Give the extent of all uninfected red blood cells.
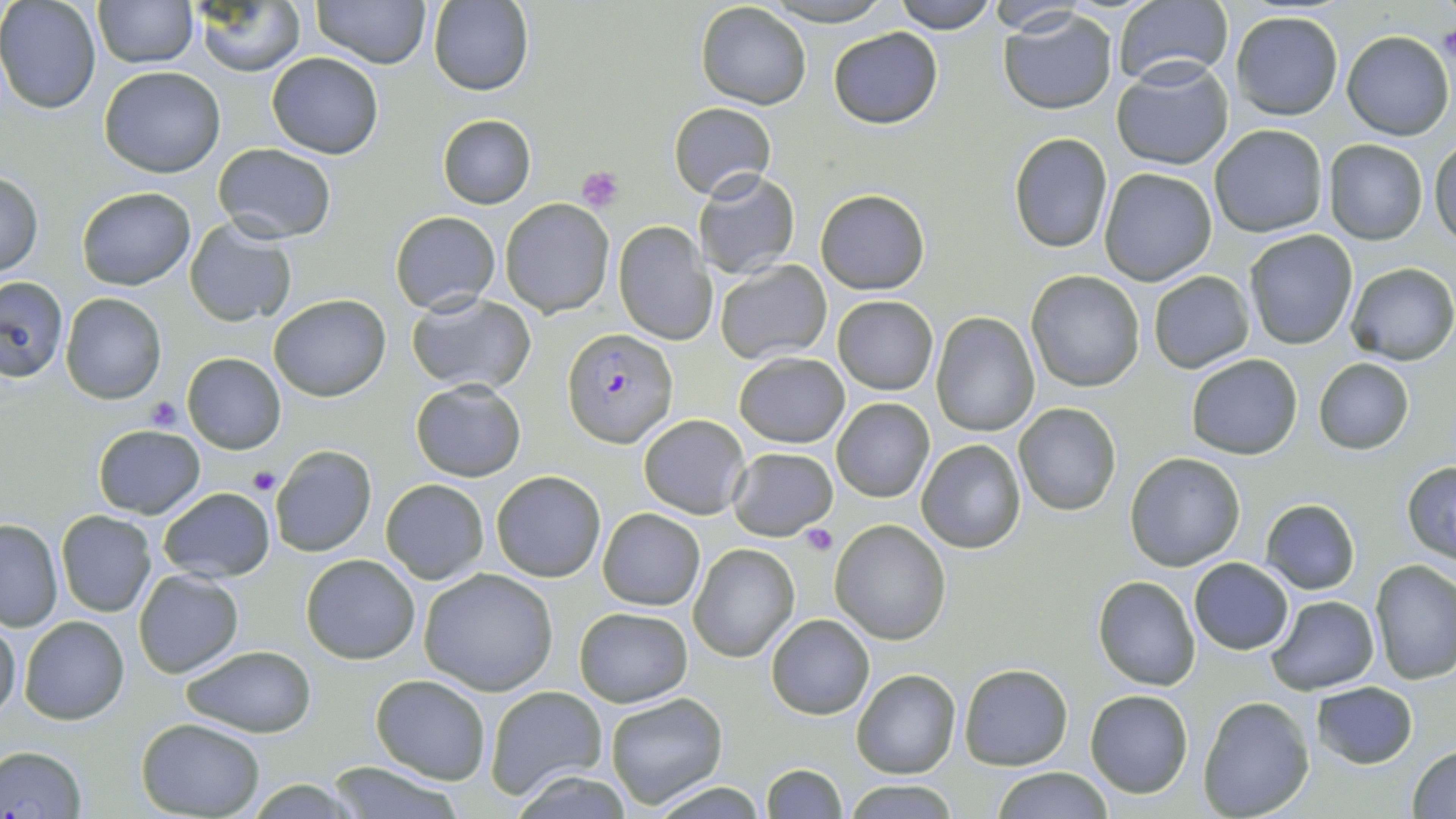

Approximate bounding boxes as (x1, y1, x2, y2) in pixels.
Uninfected red blood cells: (95, 0, 197, 67), (190, 0, 308, 75), (313, 0, 431, 69), (758, 0, 897, 25), (893, 0, 998, 33), (1111, 0, 1233, 90), (0, 1, 102, 115), (428, 1, 535, 96), (696, 2, 810, 110), (980, 2, 1091, 34), (1000, 8, 1118, 114), (1228, 10, 1344, 120), (827, 26, 943, 128), (1341, 30, 1453, 140), (266, 52, 384, 158), (1112, 58, 1235, 170), (99, 65, 225, 177), (668, 102, 776, 200), (438, 114, 535, 208), (1210, 124, 1328, 237), (1008, 133, 1114, 254), (1431, 138, 1456, 249), (1323, 139, 1430, 245), (213, 142, 337, 242), (1098, 166, 1218, 285), (0, 171, 43, 277), (695, 171, 800, 278), (76, 186, 195, 289), (815, 189, 930, 294), (501, 199, 613, 317), (390, 212, 500, 314), (184, 218, 298, 329), (613, 222, 715, 346), (1242, 229, 1358, 350), (714, 259, 833, 365), (1346, 262, 1456, 365), (1025, 270, 1146, 392), (1148, 271, 1254, 372), (0, 275, 67, 381), (406, 291, 538, 395), (60, 292, 167, 404), (268, 294, 391, 403), (832, 294, 938, 394), (929, 310, 1040, 436), (734, 352, 849, 449), (183, 354, 287, 453), (1185, 354, 1303, 459), (1312, 358, 1415, 454), (410, 379, 526, 482), (832, 397, 933, 503), (1013, 403, 1121, 516), (639, 414, 750, 519), (92, 424, 205, 519), (916, 438, 1029, 553), (269, 444, 376, 558), (727, 446, 838, 540), (1125, 452, 1247, 571), (1402, 460, 1456, 563), (491, 470, 605, 583), (380, 478, 489, 584), (158, 486, 275, 582), (1260, 498, 1361, 595), (597, 508, 705, 610), (56, 511, 157, 617), (0, 518, 63, 630), (830, 519, 952, 645), (688, 542, 801, 662), (300, 553, 420, 665), (1189, 557, 1294, 655), (1370, 559, 1456, 684), (418, 567, 558, 695), (134, 569, 244, 678), (1093, 575, 1201, 690), (1265, 595, 1380, 695), (574, 606, 692, 707), (766, 613, 874, 719), (20, 615, 131, 724), (0, 616, 23, 721), (178, 644, 316, 739), (958, 663, 1072, 769), (851, 667, 960, 778), (370, 674, 491, 784), (1309, 683, 1418, 769), (483, 685, 609, 802), (1085, 689, 1193, 797), (603, 692, 727, 809), (1198, 696, 1315, 819), (137, 718, 265, 817), (0, 744, 88, 818), (1408, 744, 1456, 818), (321, 761, 471, 817), (760, 763, 844, 819), (993, 767, 1112, 819), (842, 781, 957, 817).

slide-level diagnosis = Plasmodium falciparum
magnification = 1000x
field of view = single
platelet locations = approximate bounding boxes as (x1, y1, x2, y2) in pixels: (1434, 23, 1456, 69), (574, 165, 625, 211), (144, 395, 188, 433), (248, 468, 280, 496), (798, 524, 838, 556)
stain = May-Grünwald-Giemsa
modality = optical microscopy
Plasmodium falciparum-infected red blood cell locations = approximate bounding boxes as (x1, y1, x2, y2) in pixels: (563, 328, 679, 449)
image size = 1456×819 pixels
preparation = thin blood smear